Report the malaria status of this cell.
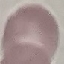

It is uninfected.

Thin smear of blood. Acquired by smartphone through the microscope eyepiece. Giemsa-stained preparation. Automatically extracted cell patch, resized to 64 × 64 pixels.